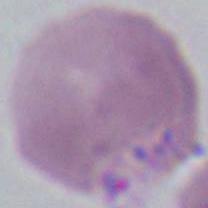
An erythrocyte is seen. 1000x magnification. Micrograph.